Describe the morphology of the erythrocytes.
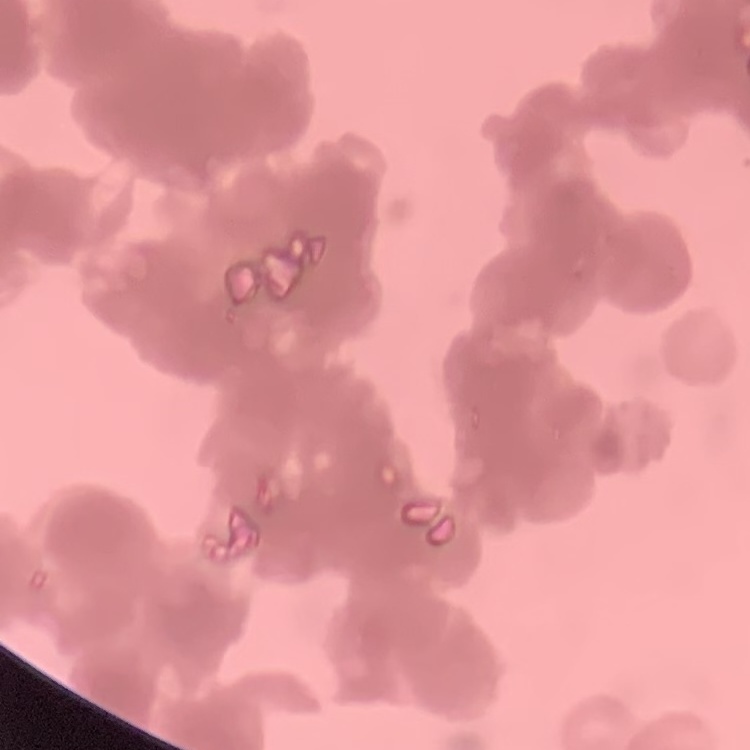

They show rouleaux formation.

Summary:
  - Stain: Field's or Giemsa
  - Preparation: thin peripheral smear
  - Image type: square crop of a larger photomicrograph